Classify this cell by malaria status.
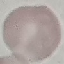
It is uninfected.

Thin blood smear. Giemsa-stained preparation. Acquired by smartphone through the microscope eyepiece. Cell patch, automatically extracted from a larger field of view and resized to 64 × 64 pixels.